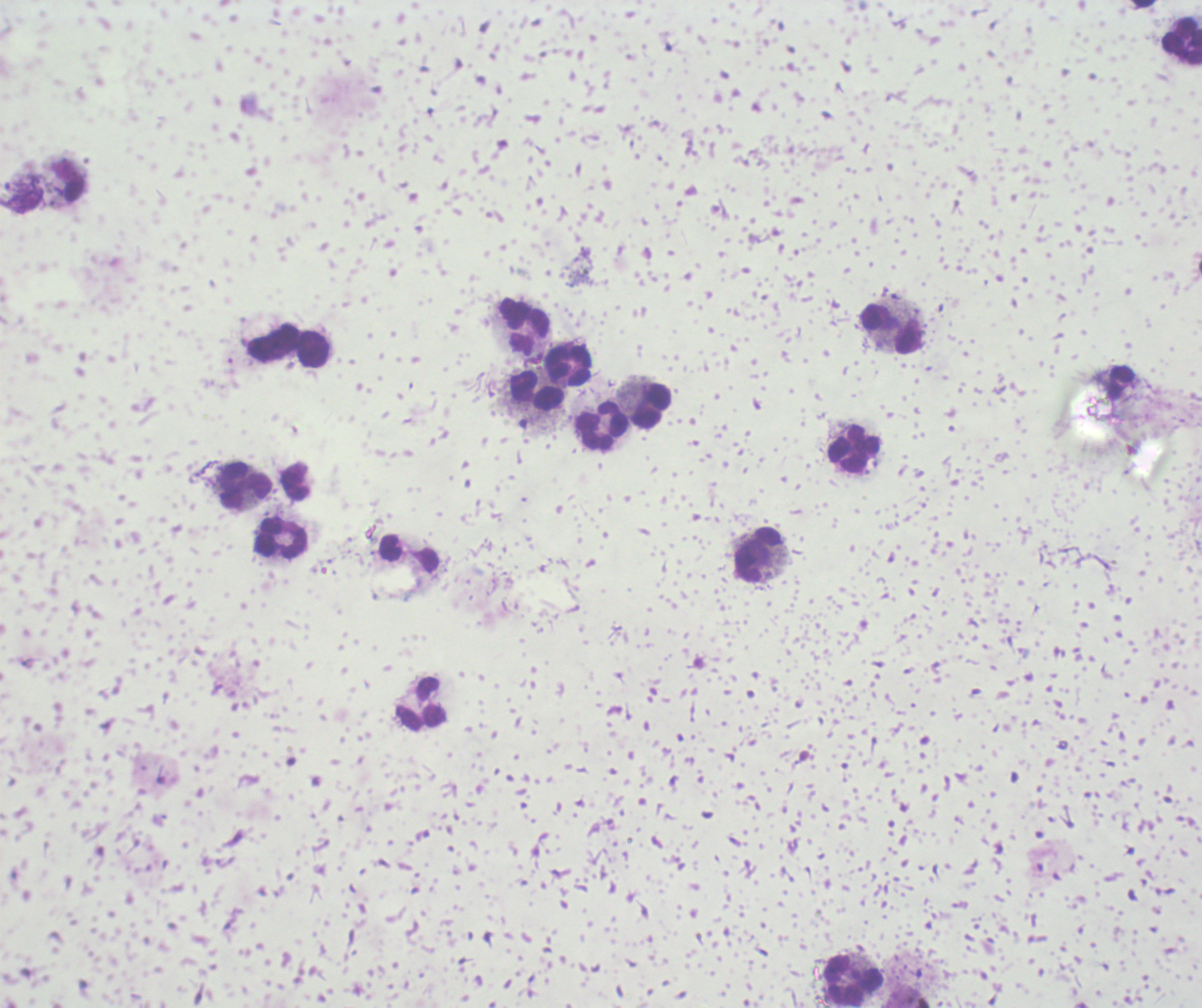
result: negative for malaria parasites
context: previously used in a real diagnosis
leukocyte_locations: 'approximate centers as [x, y] in pixels: [1181, 42], [68, 180], [525, 327], [891, 329], [271, 341], [314, 350], [567, 365], [538, 393], [650, 405], [601, 427], [853, 450], [244, 486], [281, 538], [758, 556], [423, 704], [853, 977]'
stain: Romanowsky
preparation: thick blood film
field_of_view: one from this slide
magnification: 100x
background_quality: unsatisfactory
image_size: 1202×1008 pixels